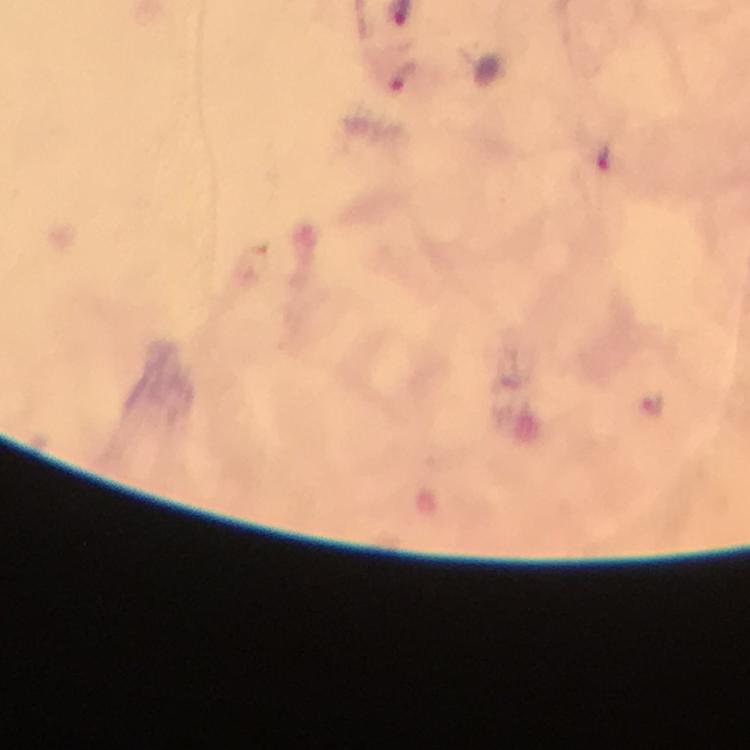

malaria parasite locations = approximate centers as {x, y} in pixels: {656, 403}
preparation = thick blood film
immersion oil = applied
cropped from = a single field of view
capture = smartphone photograph through a microscope
context = from a diagnostic examination for malaria
stain = Giemsa
magnification = 100x
image size = 750×750 pixels